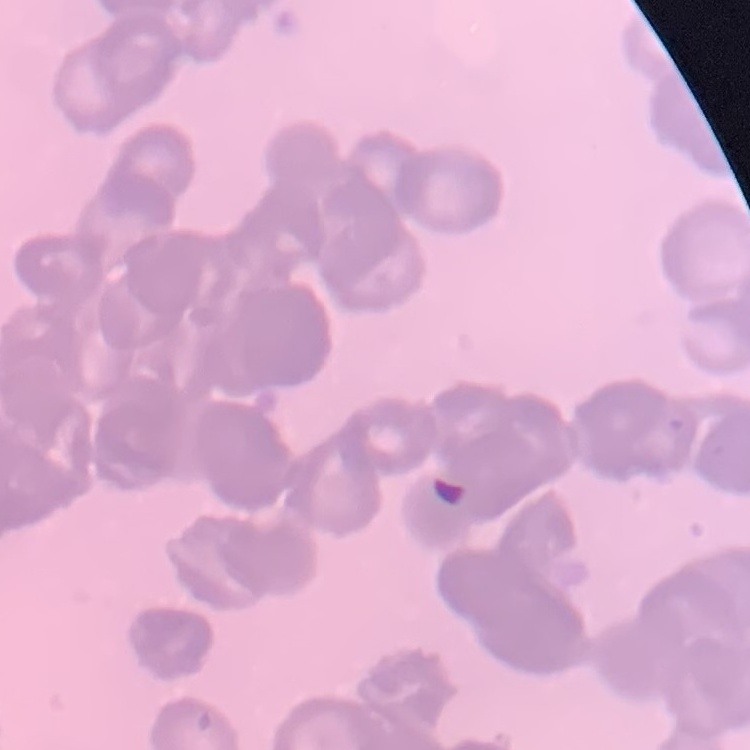

red blood cell morphology = rouleaux formation
stain = Field's or Giemsa
image type = one tile cut from a larger photomicrograph
preparation = thin blood smear